Locate platelets.
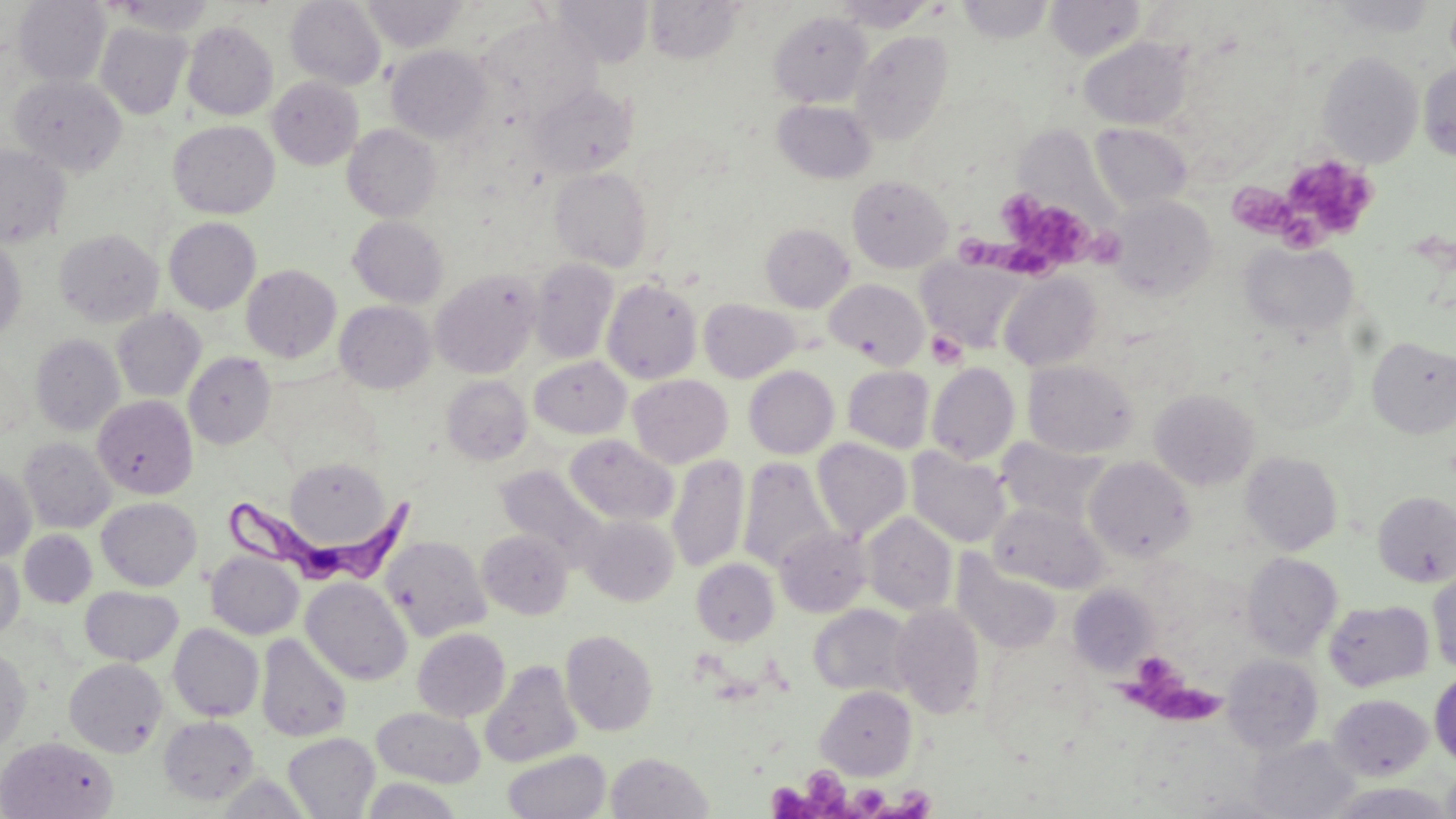

Approximate bounding boxes as named x1/y1/x2/y2 corners in pixels.
Platelets: (x1=1282, y1=154, x2=1380, y2=241), (x1=1235, y1=185, x2=1295, y2=238), (x1=1007, y1=198, x2=1123, y2=270), (x1=956, y1=225, x2=1023, y2=265), (x1=925, y1=330, x2=967, y2=370), (x1=1121, y1=657, x2=1225, y2=726), (x1=810, y1=770, x2=859, y2=819), (x1=768, y1=774, x2=818, y2=819), (x1=855, y1=782, x2=892, y2=818), (x1=894, y1=787, x2=935, y2=816).

{
  "slide_level_diagnosis": "Trypanosoma brucei",
  "image_size": "1456×819 pixels",
  "uninfected_red_blood_cell_locations": "approximate bounding boxes as named x1/y1/x2/y2 corners in pixels: (x1=14, y1=0, x2=111, y2=86), (x1=107, y1=0, x2=218, y2=36), (x1=549, y1=0, x2=654, y2=67), (x1=833, y1=0, x2=937, y2=32), (x1=285, y1=1, x2=386, y2=90), (x1=360, y1=1, x2=467, y2=51), (x1=645, y1=1, x2=744, y2=64), (x1=956, y1=1, x2=1054, y2=43), (x1=1047, y1=1, x2=1146, y2=60), (x1=1324, y1=1, x2=1439, y2=37), (x1=769, y1=11, x2=872, y2=108), (x1=476, y1=16, x2=601, y2=125), (x1=95, y1=21, x2=192, y2=119), (x1=182, y1=21, x2=278, y2=120), (x1=850, y1=30, x2=954, y2=144), (x1=1079, y1=37, x2=1192, y2=130), (x1=386, y1=45, x2=493, y2=143), (x1=1316, y1=50, x2=1423, y2=167), (x1=1419, y1=65, x2=1456, y2=161), (x1=10, y1=75, x2=127, y2=176), (x1=268, y1=77, x2=363, y2=169), (x1=529, y1=84, x2=637, y2=179), (x1=772, y1=100, x2=876, y2=183), (x1=168, y1=120, x2=279, y2=219), (x1=1090, y1=123, x2=1192, y2=211), (x1=343, y1=124, x2=442, y2=222), (x1=0, y1=145, x2=70, y2=248), (x1=549, y1=168, x2=654, y2=271), (x1=847, y1=174, x2=953, y2=273), (x1=1108, y1=195, x2=1218, y2=301), (x1=348, y1=216, x2=448, y2=308), (x1=164, y1=217, x2=261, y2=314), (x1=760, y1=223, x2=855, y2=312), (x1=54, y1=228, x2=163, y2=327), (x1=0, y1=236, x2=26, y2=344), (x1=1241, y1=241, x2=1358, y2=338), (x1=918, y1=256, x2=1029, y2=353), (x1=529, y1=259, x2=619, y2=364), (x1=241, y1=264, x2=341, y2=363), (x1=431, y1=270, x2=539, y2=378), (x1=998, y1=271, x2=1102, y2=371), (x1=601, y1=278, x2=702, y2=383), (x1=824, y1=279, x2=929, y2=368), (x1=698, y1=298, x2=800, y2=382), (x1=334, y1=300, x2=435, y2=393), (x1=112, y1=308, x2=206, y2=402), (x1=1245, y1=328, x2=1357, y2=434), (x1=30, y1=334, x2=124, y2=435), (x1=1367, y1=337, x2=1456, y2=439), (x1=183, y1=352, x2=276, y2=449), (x1=529, y1=355, x2=631, y2=439), (x1=1023, y1=360, x2=1137, y2=458), (x1=927, y1=363, x2=1020, y2=465), (x1=744, y1=365, x2=839, y2=459), (x1=842, y1=366, x2=934, y2=453), (x1=628, y1=374, x2=732, y2=467), (x1=441, y1=376, x2=532, y2=465), (x1=1149, y1=388, x2=1260, y2=490), (x1=91, y1=395, x2=197, y2=498), (x1=564, y1=434, x2=678, y2=526), (x1=995, y1=436, x2=1109, y2=525), (x1=19, y1=437, x2=115, y2=532), (x1=811, y1=438, x2=911, y2=540), (x1=907, y1=448, x2=1012, y2=548), (x1=1240, y1=451, x2=1343, y2=555), (x1=667, y1=454, x2=749, y2=573), (x1=738, y1=457, x2=838, y2=574), (x1=1085, y1=457, x2=1194, y2=562), (x1=281, y1=458, x2=394, y2=551), (x1=495, y1=465, x2=609, y2=566), (x1=0, y1=467, x2=36, y2=561), (x1=1373, y1=490, x2=1456, y2=586), (x1=96, y1=497, x2=201, y2=591), (x1=989, y1=501, x2=1107, y2=593), (x1=862, y1=512, x2=957, y2=615), (x1=579, y1=515, x2=678, y2=606), (x1=774, y1=526, x2=872, y2=617), (x1=19, y1=530, x2=97, y2=608), (x1=477, y1=530, x2=573, y2=619), (x1=381, y1=535, x2=491, y2=640), (x1=206, y1=551, x2=304, y2=639), (x1=1242, y1=552, x2=1342, y2=659), (x1=952, y1=553, x2=1063, y2=655), (x1=0, y1=555, x2=24, y2=642), (x1=691, y1=558, x2=779, y2=645), (x1=1428, y1=569, x2=1456, y2=674), (x1=301, y1=577, x2=412, y2=685), (x1=1068, y1=584, x2=1159, y2=674), (x1=80, y1=586, x2=183, y2=666), (x1=1324, y1=599, x2=1433, y2=692), (x1=891, y1=603, x2=986, y2=719), (x1=809, y1=605, x2=915, y2=698), (x1=168, y1=623, x2=264, y2=721), (x1=412, y1=628, x2=510, y2=721), (x1=561, y1=629, x2=658, y2=736), (x1=255, y1=633, x2=352, y2=743), (x1=0, y1=647, x2=31, y2=753), (x1=1223, y1=654, x2=1323, y2=754), (x1=64, y1=658, x2=167, y2=758), (x1=479, y1=660, x2=582, y2=769), (x1=1429, y1=671, x2=1456, y2=767), (x1=816, y1=685, x2=917, y2=779), (x1=1329, y1=693, x2=1432, y2=780), (x1=372, y1=707, x2=485, y2=787), (x1=158, y1=715, x2=260, y2=805), (x1=283, y1=733, x2=380, y2=818), (x1=0, y1=736, x2=118, y2=819), (x1=1248, y1=736, x2=1361, y2=818), (x1=502, y1=749, x2=611, y2=819), (x1=606, y1=751, x2=713, y2=818), (x1=1441, y1=767, x2=1456, y2=819), (x1=359, y1=777, x2=462, y2=819), (x1=1327, y1=782, x2=1455, y2=818)",
  "field_of_view": "one of a larger specimen",
  "modality": "optical microscopy",
  "trypanosoma_brucei_locations": "approximate bounding boxes as named x1/y1/x2/y2 corners in pixels: (x1=224, y1=484, x2=418, y2=586)",
  "preparation": "thin blood smear",
  "stain": "May-Grünwald-Giemsa",
  "magnification": "1000x"
}